Draw a bounding box around every parasitised red blood cell.
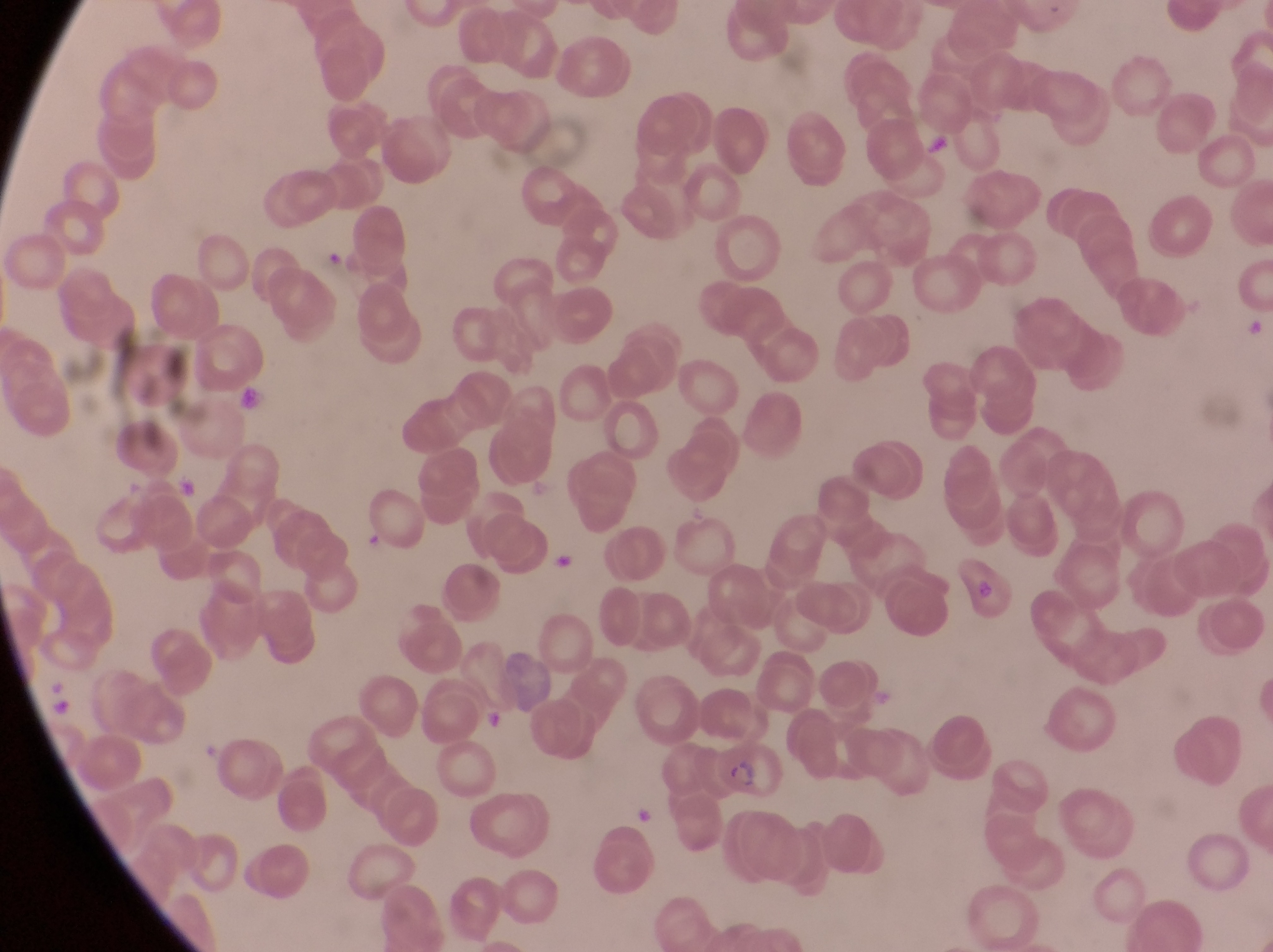
Approximate bounding boxes as [left, top, right, bottom] in pixels.
Parasitised red blood cells: [714, 739, 784, 801].

Artifact (platelet-like body, stain precipitate, or debris) locations: [236, 384, 269, 413], [633, 804, 659, 828]. Leukocyte locations: [922, 131, 953, 160], [553, 548, 577, 574], [482, 707, 510, 735]. At a magnification of 1000x. Single field of view. Thin blood smear. Image is 1273×952 pixels. Photographed through the eyepiece of an Olympus CX-23 microscope with a smartphone camera. Sample from Uganda.